Report the malaria status of this cell.
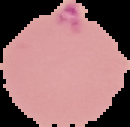
It is parasitized.

Summary:
  - Image size: 130×127 pixels
  - Preparation: thin blood film
  - Image type: segmented cell region on a black background